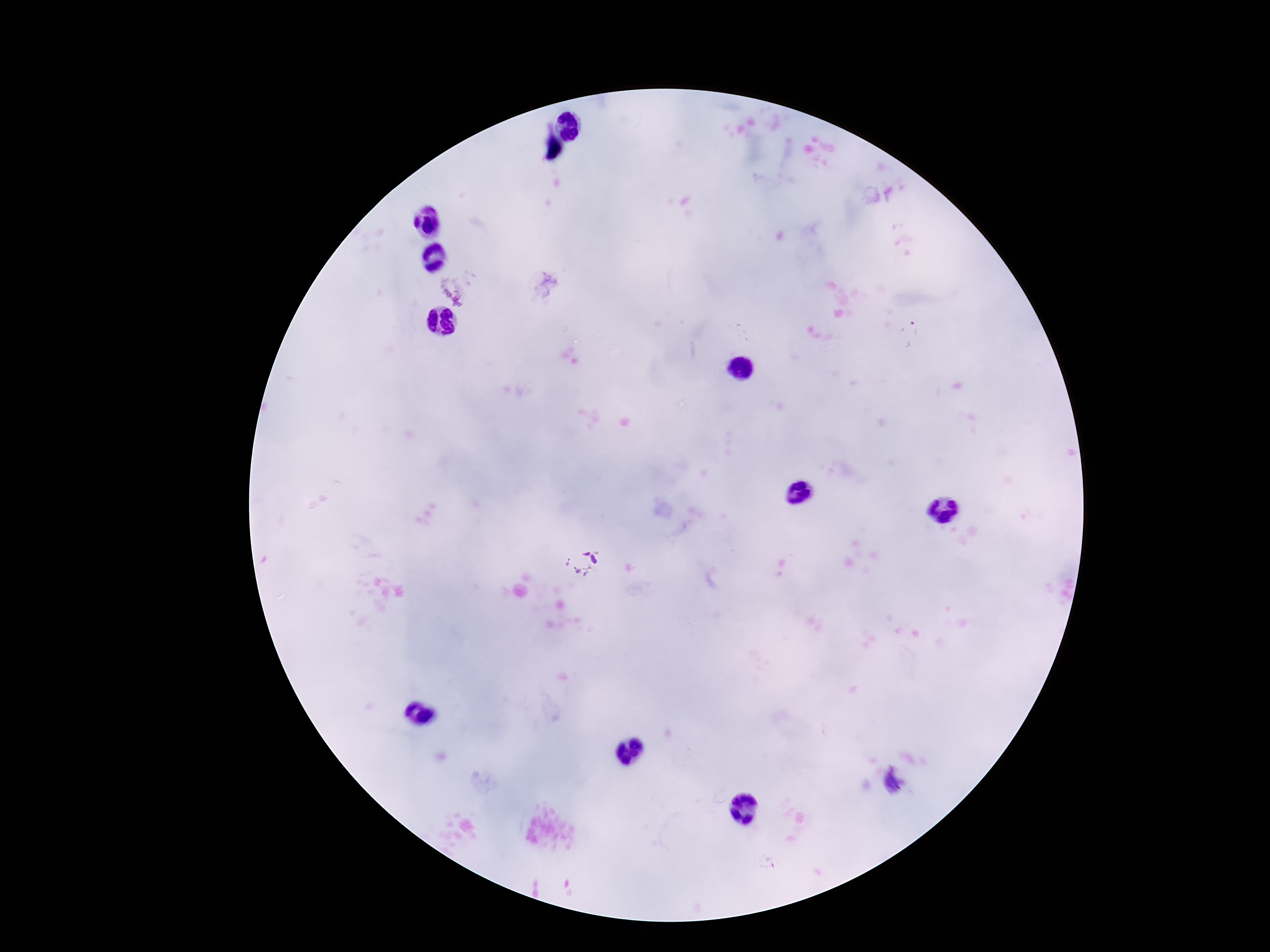
image size = 1270×952 pixels
stain = Giemsa
field of view = single
capture = smartphone camera through the microscope eyepiece
magnification = 100x
preparation = thick peripheral-blood smear
Plasmodium parasite locations = approximate object centers, in pixels from the top-left corner: (x=453, y=287), (x=580, y=561), (x=892, y=783)
patient malaria status = infected